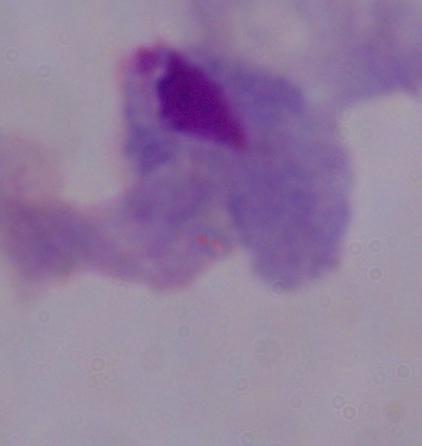
1000x magnification. Micrograph. A trichomonad is seen.